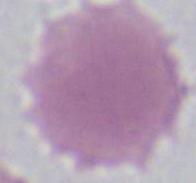

Captured at 1000x magnification. Micrograph. A red blood cell is seen.